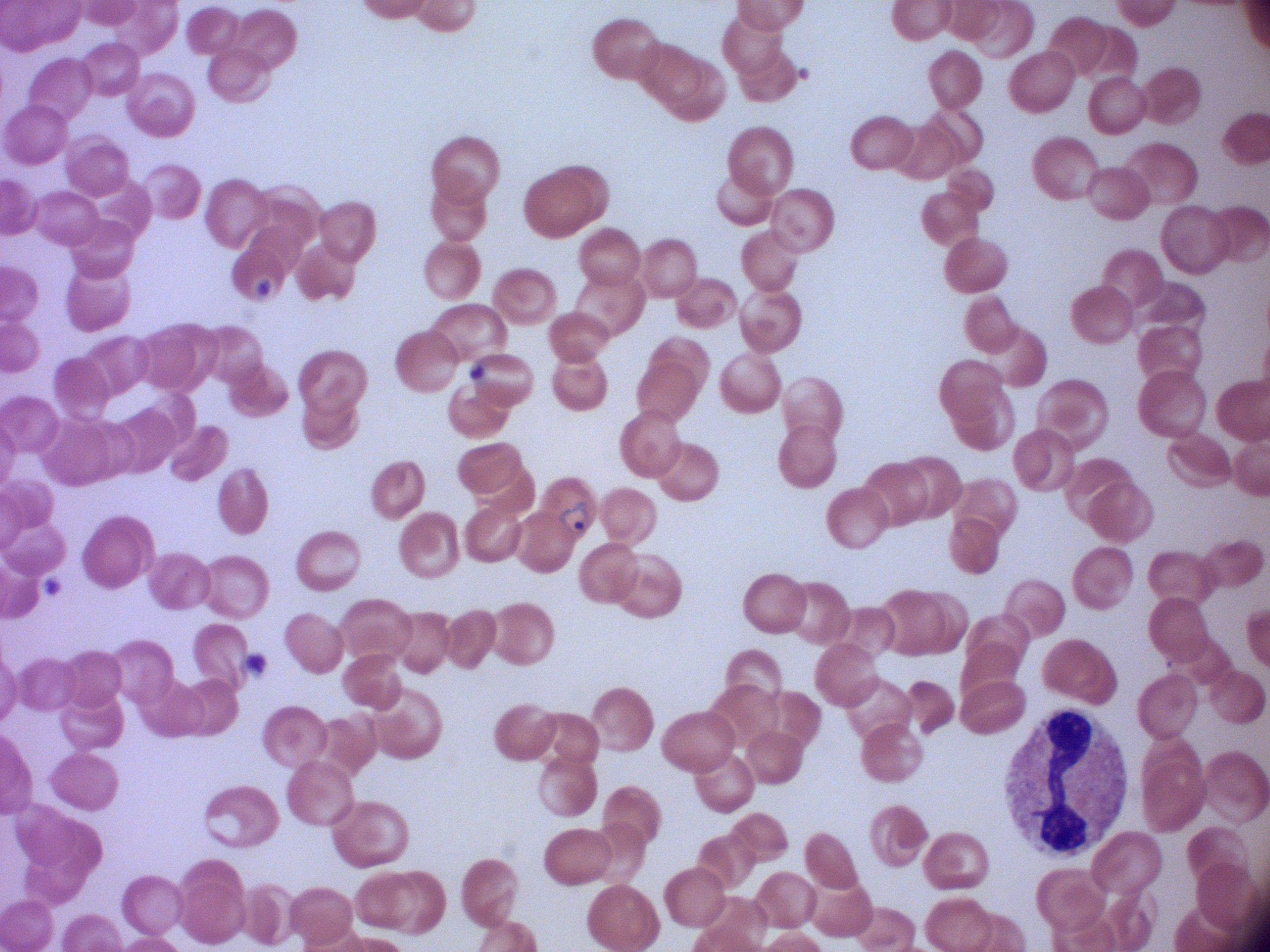

Approximate bounding boxes as (x1,y1)-(x2,y2) corner pairs in pixels, from the source annotation, which is not necessarily exhaustive. Ring form locations: (550,497)-(593,538). Image is 1270×952 pixels. One field from this slide. Captured at 100x magnification. Thin blood film. Giemsa-stained preparation. Acquired with a Leica DM2000 optical microscope and its built-in camera. Species: Plasmodium falciparum.